Locate every Plasmodium parasite.
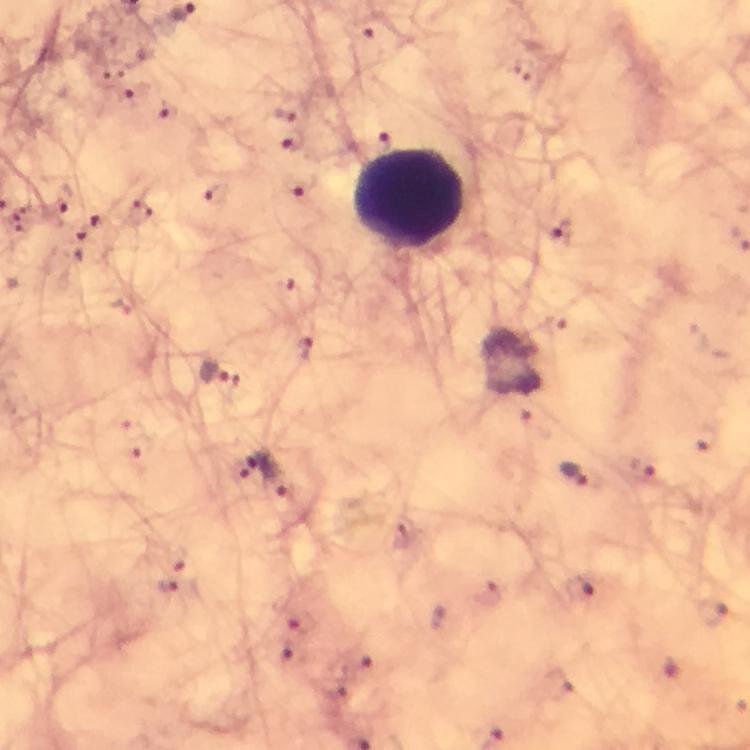

Approximate centers as (x, y) in pixels.
Plasmodium parasites: (283, 112), (292, 141), (300, 183), (64, 200), (140, 212), (100, 220), (562, 233), (80, 242), (303, 348), (222, 377), (251, 464), (643, 472), (574, 474).

Summary:
  - Leukocyte locations: (409, 196)
  - Context: from a malaria diagnostic workup
  - Cropped from: one field of view
  - Stain: Giemsa
  - Image size: 750×750 pixels
  - Capture: smartphone camera through the microscope
  - Preparation: thick blood film
  - Immersion oil: applied
  - Magnification: 100x